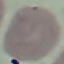

result = no malaria parasites detected
capture = smartphone camera at the microscope eyepiece
preparation = thin smear
stain = Giemsa
image type = automatically extracted cell patch, resized to 64 × 64 pixels